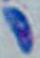

modality: micrograph
identification: Toxoplasma gondii
magnification: 1000x